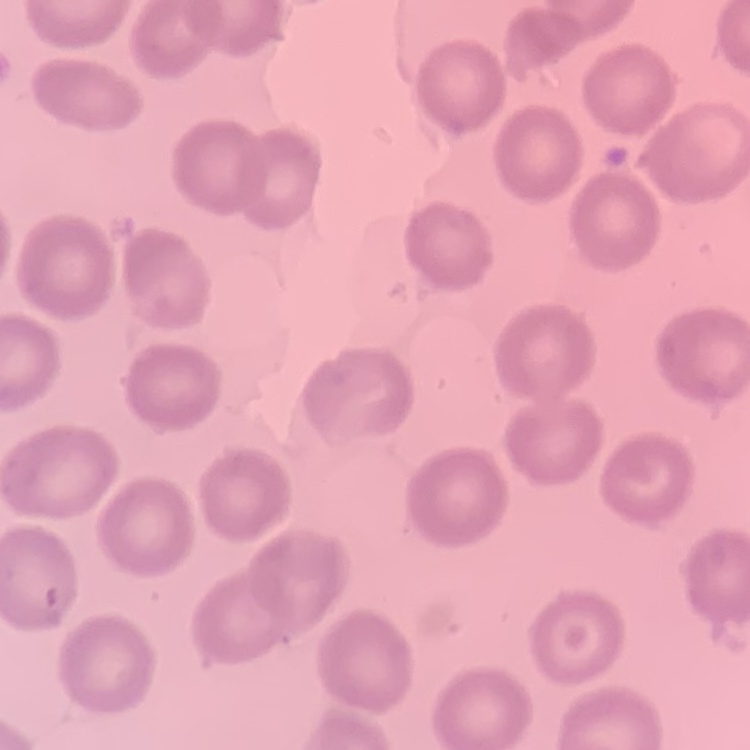

The erythrocytes exhibit no rouleaux formation. Stained with either Field's or Giemsa. Thin peripheral smear. Square crop of a larger photomicrograph.